Report the malaria status of this cell.
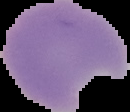
Parasitized.

The area outside the segmented cell region is set to black. From a thin blood film. Image is 130×112 pixels.